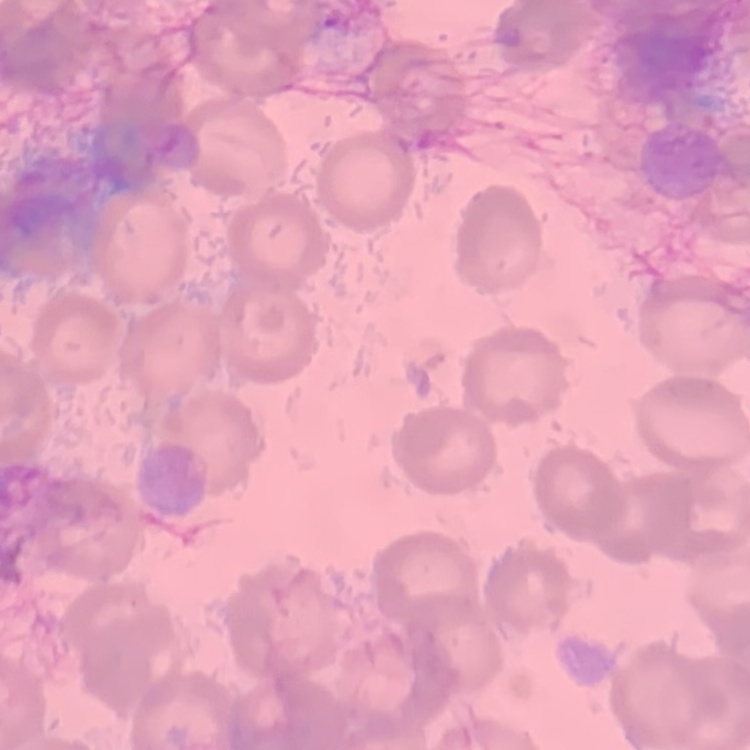

The red blood cells exhibit no rouleaux formation. Thin peripheral smear. One tile cut from a larger photomicrograph. Stained with either Field's or Giemsa.